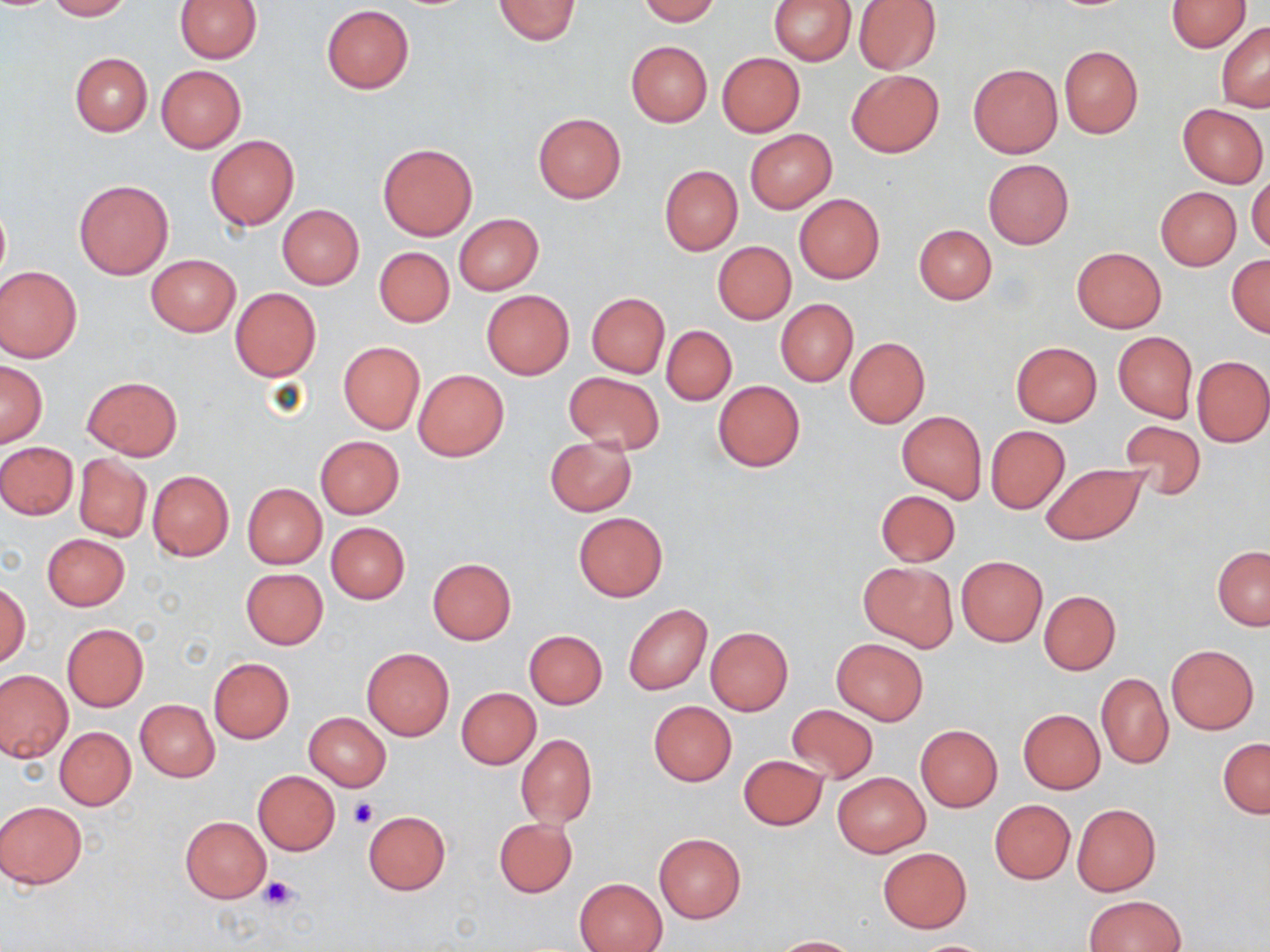

slide-level diagnosis = negative for blood parasites
modality = light microscopy
stain = May-Grünwald-Giemsa
field of view = one of a larger specimen
image size = 1270×952 pixels
preparation = thin blood film
magnification = 1000x
uninfected red blood cell locations = approximate bounding boxes as named x1/y1/x2/y2 corners in pixels: (x1=45, y1=0, x2=132, y2=20), (x1=175, y1=0, x2=261, y2=63), (x1=493, y1=0, x2=581, y2=44), (x1=638, y1=0, x2=720, y2=24), (x1=769, y1=0, x2=856, y2=64), (x1=853, y1=0, x2=941, y2=74), (x1=1165, y1=1, x2=1250, y2=52), (x1=321, y1=4, x2=414, y2=93), (x1=1217, y1=21, x2=1270, y2=110), (x1=626, y1=41, x2=712, y2=126), (x1=1059, y1=46, x2=1143, y2=138), (x1=716, y1=52, x2=805, y2=137), (x1=69, y1=53, x2=153, y2=136), (x1=969, y1=64, x2=1062, y2=158), (x1=156, y1=65, x2=246, y2=153), (x1=846, y1=70, x2=944, y2=157), (x1=1178, y1=103, x2=1268, y2=187), (x1=533, y1=113, x2=626, y2=203), (x1=746, y1=130, x2=836, y2=213), (x1=205, y1=135, x2=299, y2=230), (x1=378, y1=143, x2=477, y2=239), (x1=983, y1=159, x2=1074, y2=248), (x1=659, y1=165, x2=742, y2=255), (x1=1248, y1=172, x2=1270, y2=253), (x1=73, y1=178, x2=174, y2=280), (x1=1155, y1=186, x2=1241, y2=269), (x1=794, y1=193, x2=885, y2=283), (x1=1, y1=204, x2=9, y2=284), (x1=277, y1=205, x2=364, y2=289), (x1=454, y1=213, x2=544, y2=294), (x1=913, y1=224, x2=996, y2=304), (x1=712, y1=243, x2=796, y2=324), (x1=374, y1=247, x2=454, y2=327), (x1=1071, y1=247, x2=1166, y2=332), (x1=1227, y1=254, x2=1270, y2=337), (x1=147, y1=255, x2=240, y2=336), (x1=0, y1=266, x2=82, y2=362), (x1=230, y1=287, x2=321, y2=382), (x1=482, y1=290, x2=573, y2=378), (x1=586, y1=292, x2=669, y2=378), (x1=775, y1=299, x2=858, y2=387), (x1=662, y1=326, x2=736, y2=405), (x1=1113, y1=332, x2=1197, y2=421), (x1=845, y1=338, x2=930, y2=427), (x1=338, y1=340, x2=425, y2=434), (x1=1011, y1=342, x2=1102, y2=426), (x1=1192, y1=355, x2=1269, y2=447), (x1=0, y1=360, x2=47, y2=447), (x1=414, y1=369, x2=509, y2=460), (x1=564, y1=372, x2=664, y2=453), (x1=82, y1=375, x2=182, y2=459), (x1=713, y1=380, x2=805, y2=471), (x1=896, y1=410, x2=986, y2=503), (x1=1116, y1=420, x2=1207, y2=500), (x1=986, y1=425, x2=1070, y2=513), (x1=315, y1=436, x2=404, y2=518), (x1=544, y1=436, x2=636, y2=515), (x1=0, y1=441, x2=78, y2=519), (x1=73, y1=454, x2=151, y2=542), (x1=1040, y1=464, x2=1148, y2=545), (x1=148, y1=470, x2=234, y2=561), (x1=243, y1=484, x2=327, y2=568), (x1=876, y1=490, x2=961, y2=566), (x1=574, y1=512, x2=667, y2=601), (x1=326, y1=522, x2=410, y2=604), (x1=42, y1=533, x2=129, y2=610), (x1=1212, y1=546, x2=1270, y2=630), (x1=427, y1=557, x2=517, y2=644), (x1=957, y1=557, x2=1047, y2=645), (x1=860, y1=561, x2=956, y2=649), (x1=241, y1=568, x2=329, y2=649), (x1=1, y1=583, x2=31, y2=668), (x1=1039, y1=591, x2=1120, y2=674), (x1=624, y1=604, x2=712, y2=695), (x1=62, y1=623, x2=148, y2=711), (x1=705, y1=627, x2=793, y2=714), (x1=524, y1=630, x2=608, y2=708), (x1=830, y1=638, x2=929, y2=726), (x1=1166, y1=644, x2=1258, y2=734), (x1=361, y1=648, x2=455, y2=740), (x1=209, y1=659, x2=294, y2=742), (x1=0, y1=670, x2=73, y2=763), (x1=1096, y1=672, x2=1174, y2=769), (x1=456, y1=688, x2=540, y2=769), (x1=135, y1=699, x2=220, y2=781), (x1=649, y1=701, x2=736, y2=785), (x1=785, y1=704, x2=877, y2=783), (x1=1017, y1=709, x2=1104, y2=794), (x1=304, y1=712, x2=391, y2=791), (x1=915, y1=724, x2=1002, y2=811), (x1=54, y1=726, x2=136, y2=811), (x1=516, y1=733, x2=597, y2=830), (x1=1219, y1=739, x2=1270, y2=818), (x1=738, y1=755, x2=828, y2=830), (x1=253, y1=770, x2=340, y2=855), (x1=833, y1=772, x2=930, y2=857), (x1=989, y1=799, x2=1075, y2=883), (x1=1, y1=801, x2=88, y2=889), (x1=1071, y1=804, x2=1160, y2=896), (x1=362, y1=810, x2=450, y2=895), (x1=180, y1=816, x2=271, y2=903), (x1=494, y1=818, x2=577, y2=898), (x1=654, y1=834, x2=746, y2=923), (x1=877, y1=848, x2=971, y2=933), (x1=575, y1=877, x2=668, y2=952), (x1=1084, y1=895, x2=1187, y2=952), (x1=771, y1=936, x2=864, y2=951), (x1=907, y1=939, x2=999, y2=951)
platelet locations = approximate bounding boxes as named x1/y1/x2/y2 corners in pixels: (x1=348, y1=797, x2=379, y2=827), (x1=258, y1=875, x2=300, y2=911)